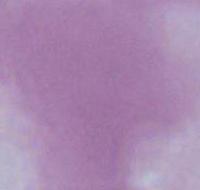

Micrograph. An erythrocyte is seen. Captured at 1000x magnification.